Identify the parasite.
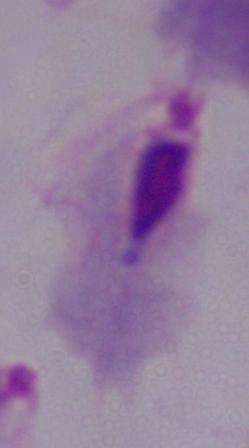

A trichomonad.

Captured at 1000x magnification. Photomicrograph.